Give the position of every Plasmodium parasite visible.
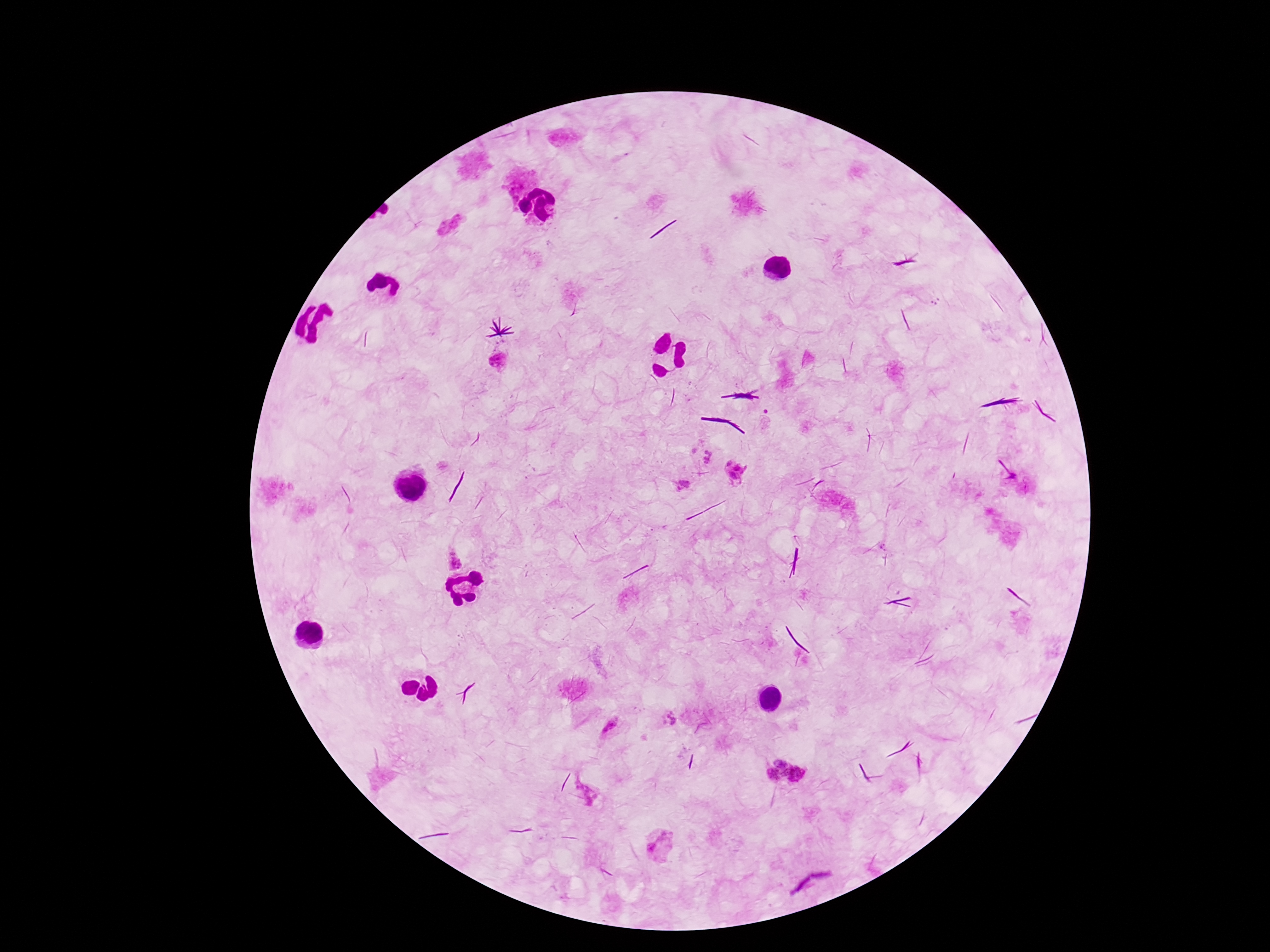

Approximate object centers, in pixels from the top-left corner.
Plasmodium parasites: (x=458, y=221), (x=442, y=227), (x=497, y=361), (x=709, y=456), (x=734, y=470), (x=685, y=480), (x=679, y=489), (x=884, y=547), (x=451, y=559), (x=666, y=718), (x=611, y=727), (x=782, y=761), (x=798, y=773), (x=772, y=776), (x=659, y=844).

Summary:
  - Stain: Giemsa
  - Magnification: 100x
  - Preparation: thick peripheral-blood smear
  - Patient malaria status: infected
  - Image size: 1270×952 pixels
  - Field of view: one from this slide
  - Capture: smartphone camera through the microscope eyepiece